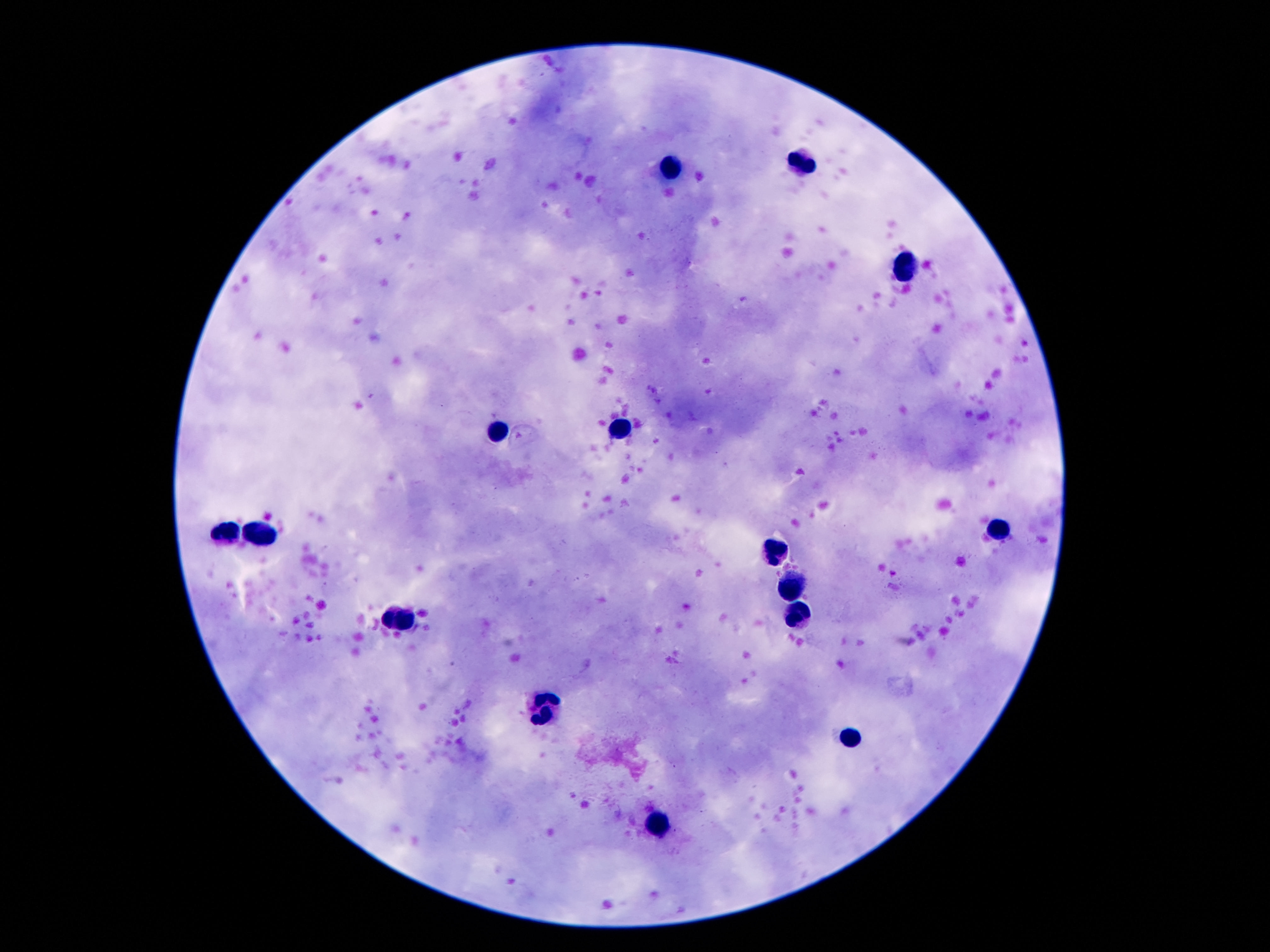

{
  "stain": "Giemsa",
  "preparation": "thick peripheral-blood smear",
  "field_of_view": "single",
  "image_size": "1270×952 pixels",
  "leukocyte_locations": "approximate object centers, in pixels from the top-left corner: (x=802, y=161), (x=667, y=166), (x=910, y=266), (x=623, y=426), (x=494, y=432), (x=998, y=533), (x=223, y=535), (x=258, y=535), (x=778, y=551), (x=793, y=586), (x=800, y=617), (x=400, y=619), (x=544, y=708), (x=850, y=738), (x=658, y=826)",
  "patient_malaria_status": "negative",
  "capture": "smartphone camera through the microscope eyepiece",
  "magnification": "100x"
}